Outline each blood parasite and name the species.
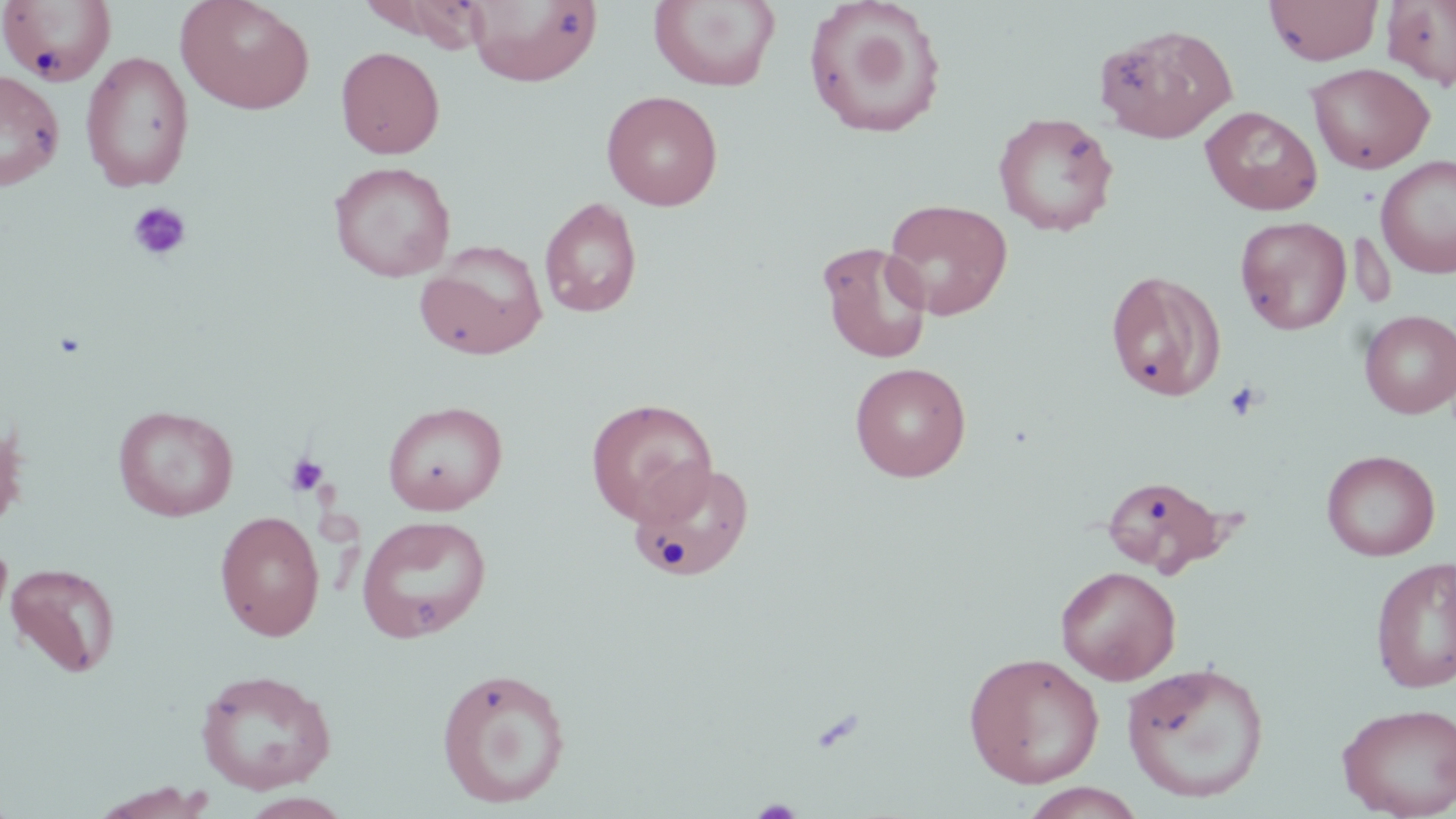

No blood parasites seen.

Summary:
  - Coordinate format: approximate bounding boxes as [x1, y1, x2, y2] in pixels
  - Uninfected red blood cell locations: [175, 0, 315, 115], [465, 0, 603, 87], [649, 0, 782, 92], [802, 0, 947, 141], [1264, 0, 1384, 66], [1383, 0, 1456, 89], [0, 1, 117, 86], [362, 1, 488, 50], [1095, 23, 1236, 143], [335, 46, 445, 159], [80, 51, 195, 192], [1306, 62, 1435, 174], [0, 68, 65, 192], [601, 90, 723, 210], [1201, 106, 1323, 215], [992, 112, 1119, 236], [1375, 155, 1456, 279], [328, 161, 456, 282], [539, 197, 643, 318], [882, 198, 1014, 321], [1234, 216, 1351, 335], [816, 240, 933, 364], [415, 241, 548, 360], [1105, 268, 1227, 402], [1359, 310, 1456, 418], [849, 362, 971, 482], [585, 398, 718, 524], [381, 401, 508, 515], [113, 405, 238, 521], [0, 413, 26, 535], [1321, 449, 1440, 561], [628, 459, 755, 582], [1100, 474, 1233, 577], [214, 510, 325, 641], [356, 514, 492, 642], [1370, 557, 1456, 694], [5, 562, 121, 679], [1055, 565, 1181, 684], [963, 651, 1105, 789], [1121, 660, 1270, 803], [435, 666, 572, 809], [195, 668, 337, 794], [1336, 702, 1456, 818], [89, 782, 216, 819], [1020, 783, 1148, 818]
  - Platelet locations: [127, 200, 192, 262], [1223, 380, 1265, 422], [283, 451, 331, 498]
  - Slide-level diagnosis: negative for blood parasites
  - Preparation: thin blood film
  - Magnification: 1000x
  - Image size: 1456×819 pixels
  - Field of view: single
  - Stain: May-Grünwald-Giemsa
  - Modality: light microscopy